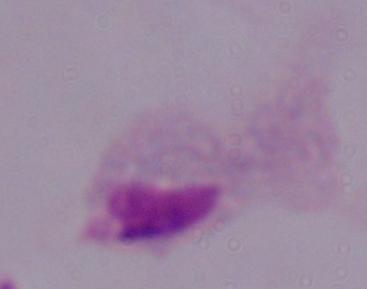
{
  "modality": "photomicrograph",
  "identification": "trichomonad",
  "magnification": "1000x"
}